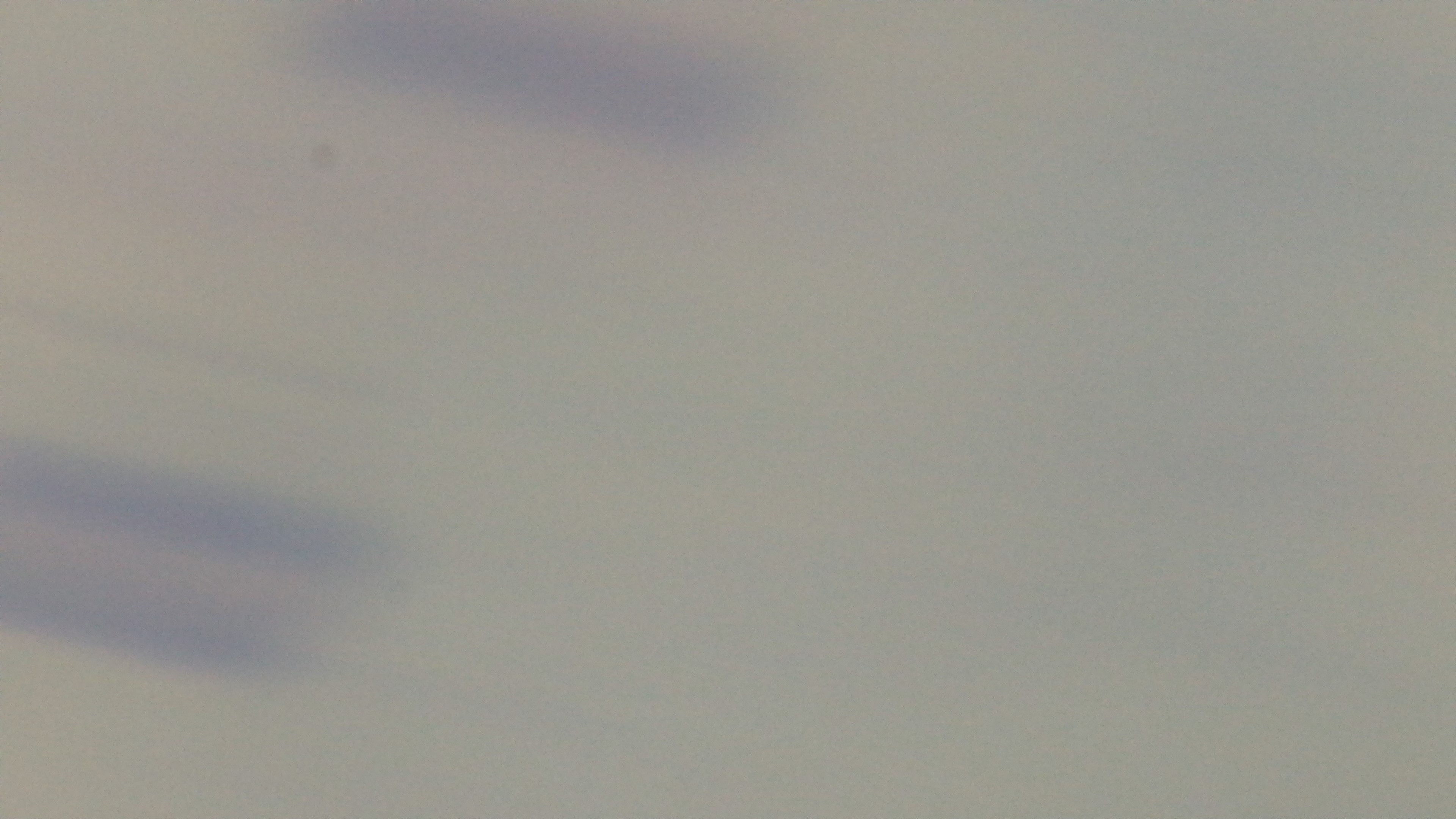
Summary:
  - Field of view: single
  - Stain: Giemsa
  - Modality: light microscopy
  - Capture: mounted 4K digital camera
  - Preparation: thick blood film
  - Malaria status: negative
  - Objective: 100x oil immersion